State which parasite is depicted.
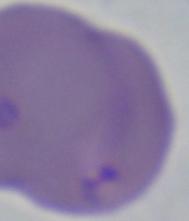
Babesia.

Photomicrograph. Captured at 1000x magnification.